Report the malaria status of this cell.
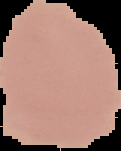
Uninfected.

Summary:
  - Preparation: thin blood smear
  - Image type: cell region segmented out of the field of view; surrounding area masked to black
  - Image size: 121×151 pixels